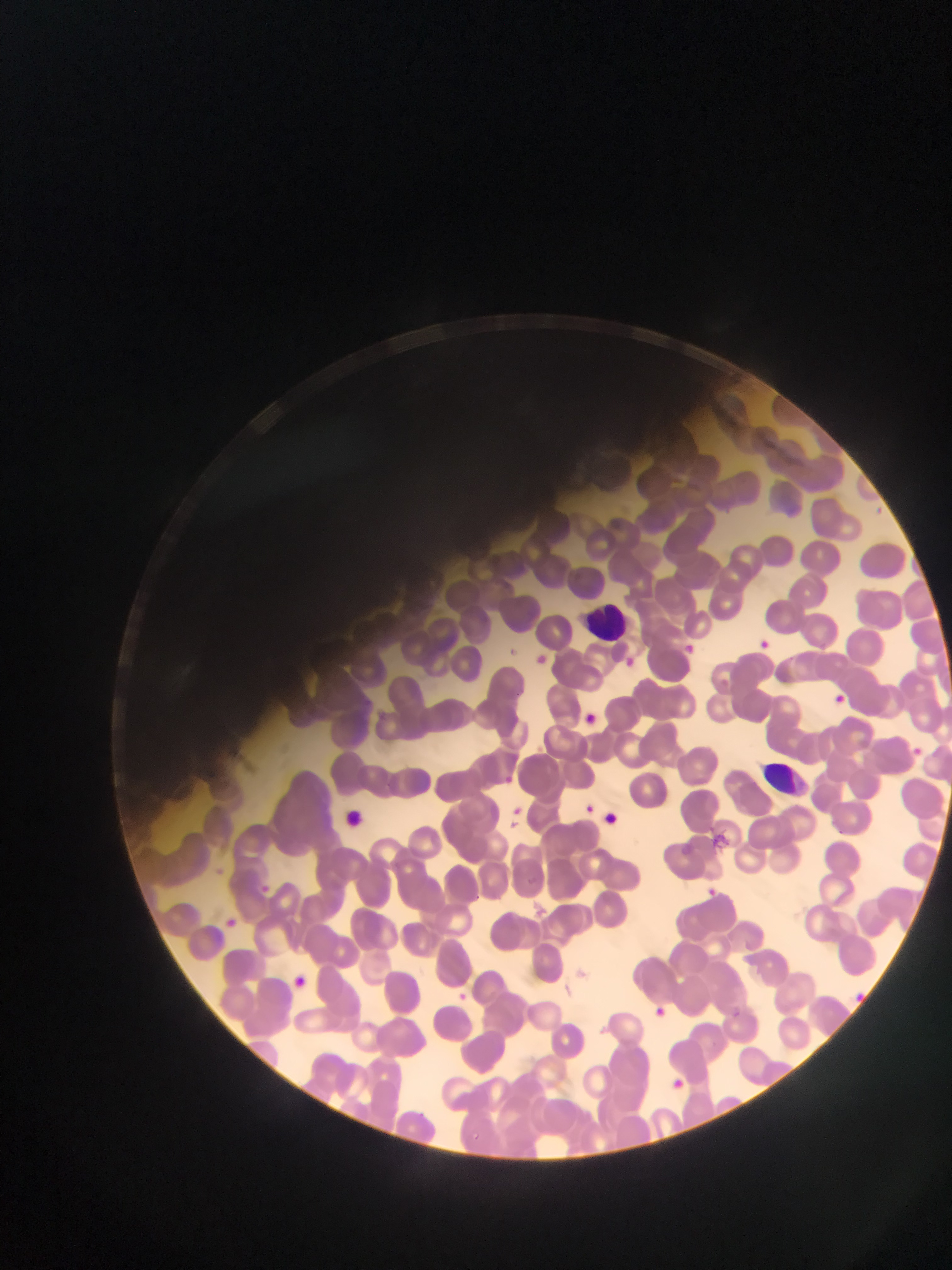

Approximate bounding boxes as (left, top, right, bottom) in pixels. Leukocyte locations: (588, 589, 638, 658), (772, 739, 815, 797). Malaria parasite locations: (753, 638, 773, 656), (680, 640, 699, 658), (614, 650, 640, 676), (530, 651, 551, 669), (828, 690, 849, 709), (577, 709, 600, 730), (911, 745, 926, 759), (496, 772, 517, 791), (582, 802, 597, 817), (503, 809, 525, 834), (601, 810, 620, 828), (700, 887, 719, 903), (220, 914, 241, 934), (285, 971, 314, 995), (448, 989, 473, 1011), (644, 1002, 669, 1024), (665, 1075, 688, 1095). Mobile-phone photograph taken through the microscope. Thin blood smear. Single field of view. Sample from Ghana. Image is 952×1270 pixels.